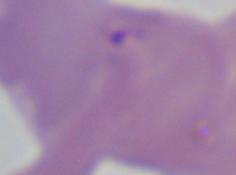

Micrograph. A Babesia parasite is shown. 1000x magnification.